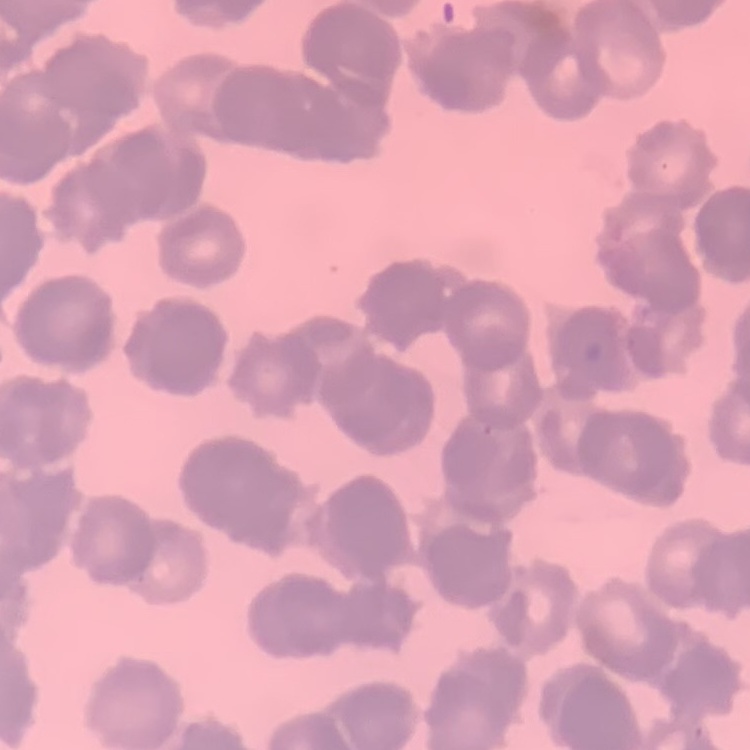

The red blood cells exhibit rouleaux formation. Stained with either Field's or Giemsa. Thin blood film. One tile cut from a larger photomicrograph.